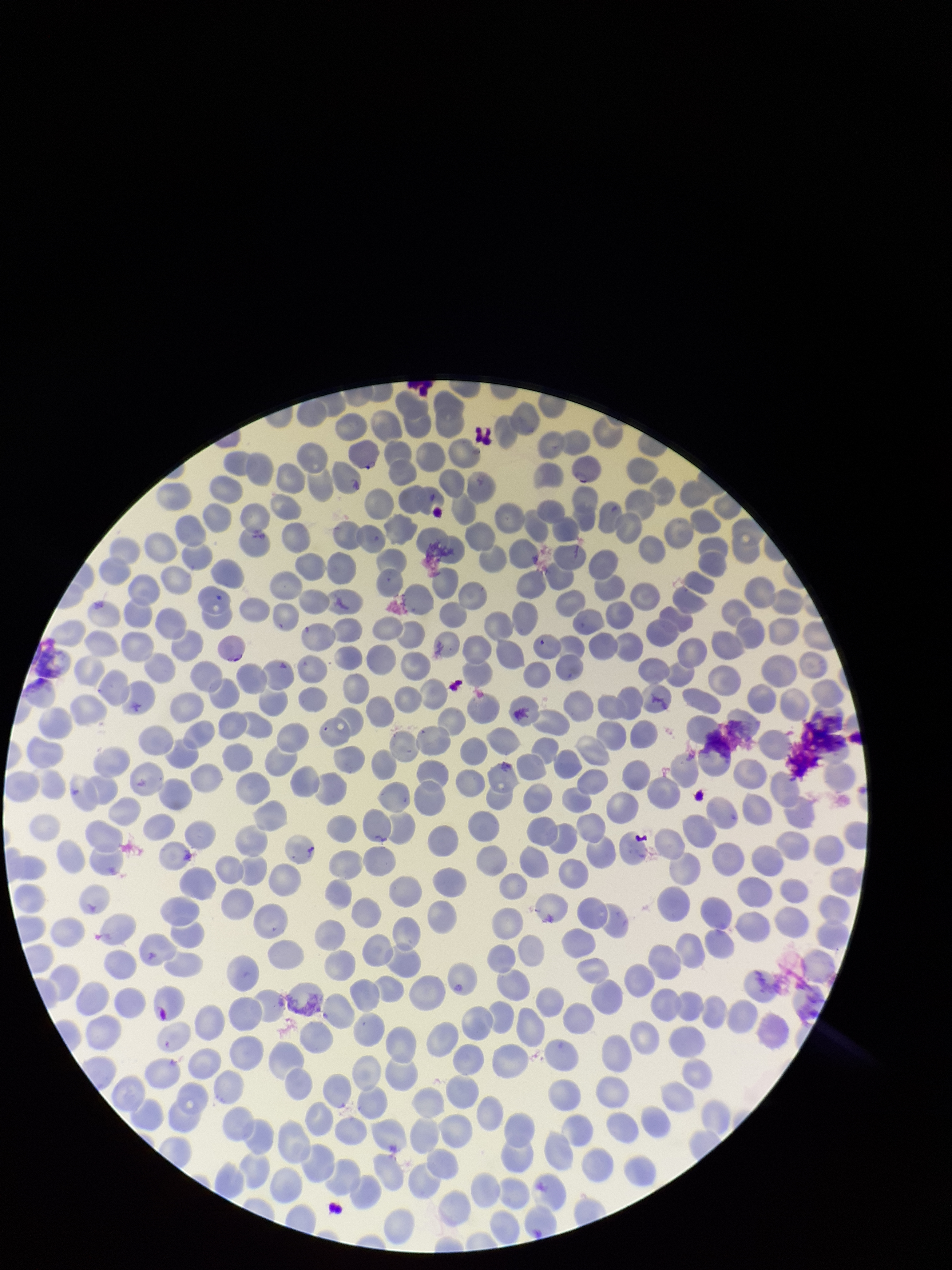

image_size: 952×1270 pixels
capture: smartphone photograph through the microscope eyepiece
parasitized_red_blood_cell_count: 1
stain: Giemsa
parasitized_red_blood_cells: seen
species_reported_for_this_patient: Plasmodium falciparum
red_blood_cell_count: 364
field_of_view: single
patient_malaria_status: positive
preparation: thin smear